Identify the preparation type.
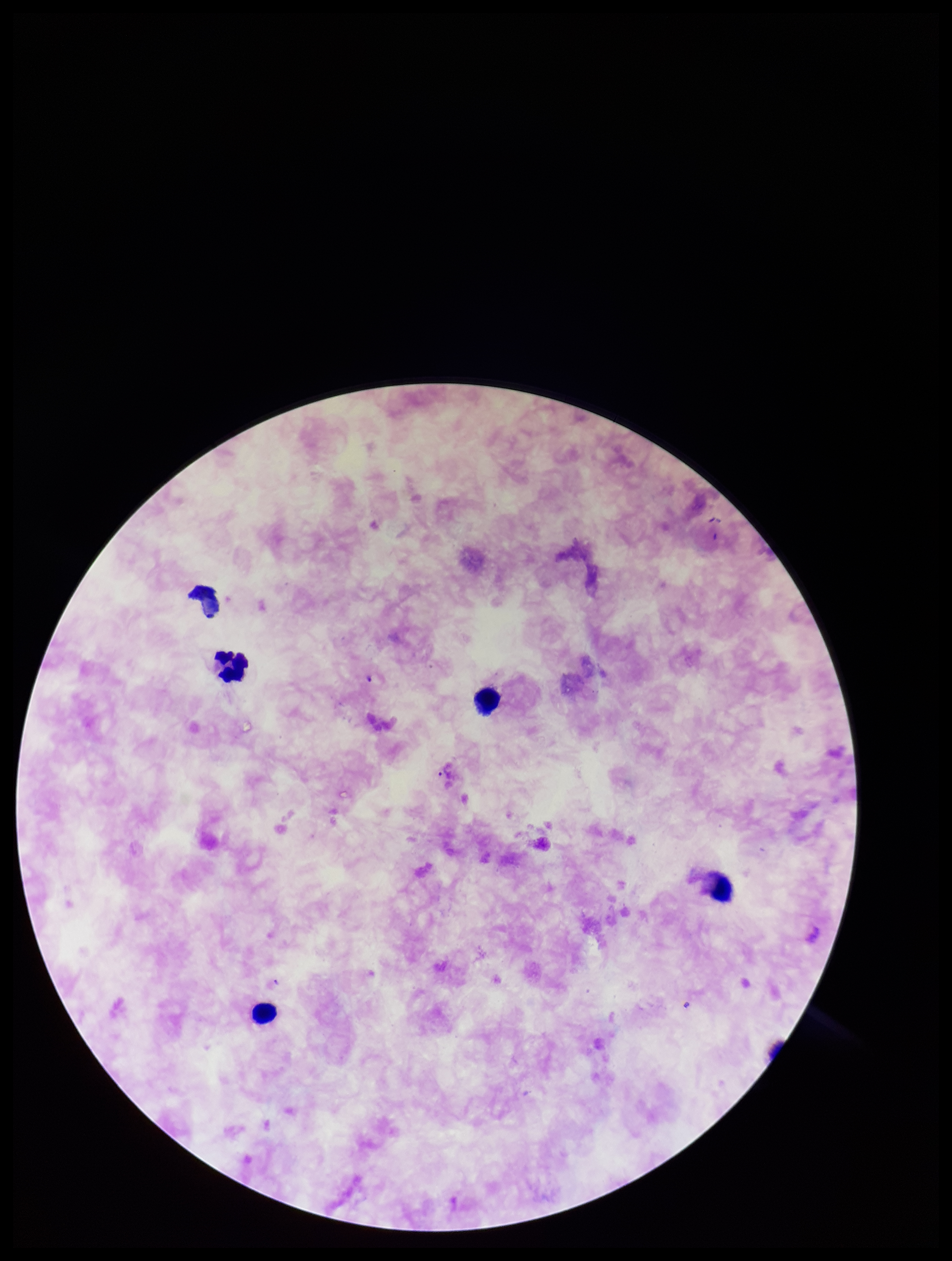
A thick smear.

Summary:
  - Patient malaria status: infected
  - Leukocyte count: 5
  - Species reported for this patient: Plasmodium falciparum
  - Field of view: one from this slide
  - Plasmodium parasites: none identified
  - Stain: Giemsa
  - Capture: smartphone photograph through the microscope eyepiece
  - Parasite count: 0
  - Image size: 952×1261 pixels